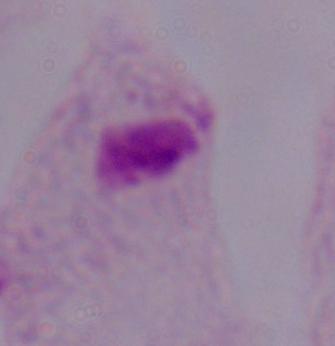

magnification = 1000x
modality = photomicrograph
identification = trichomonad